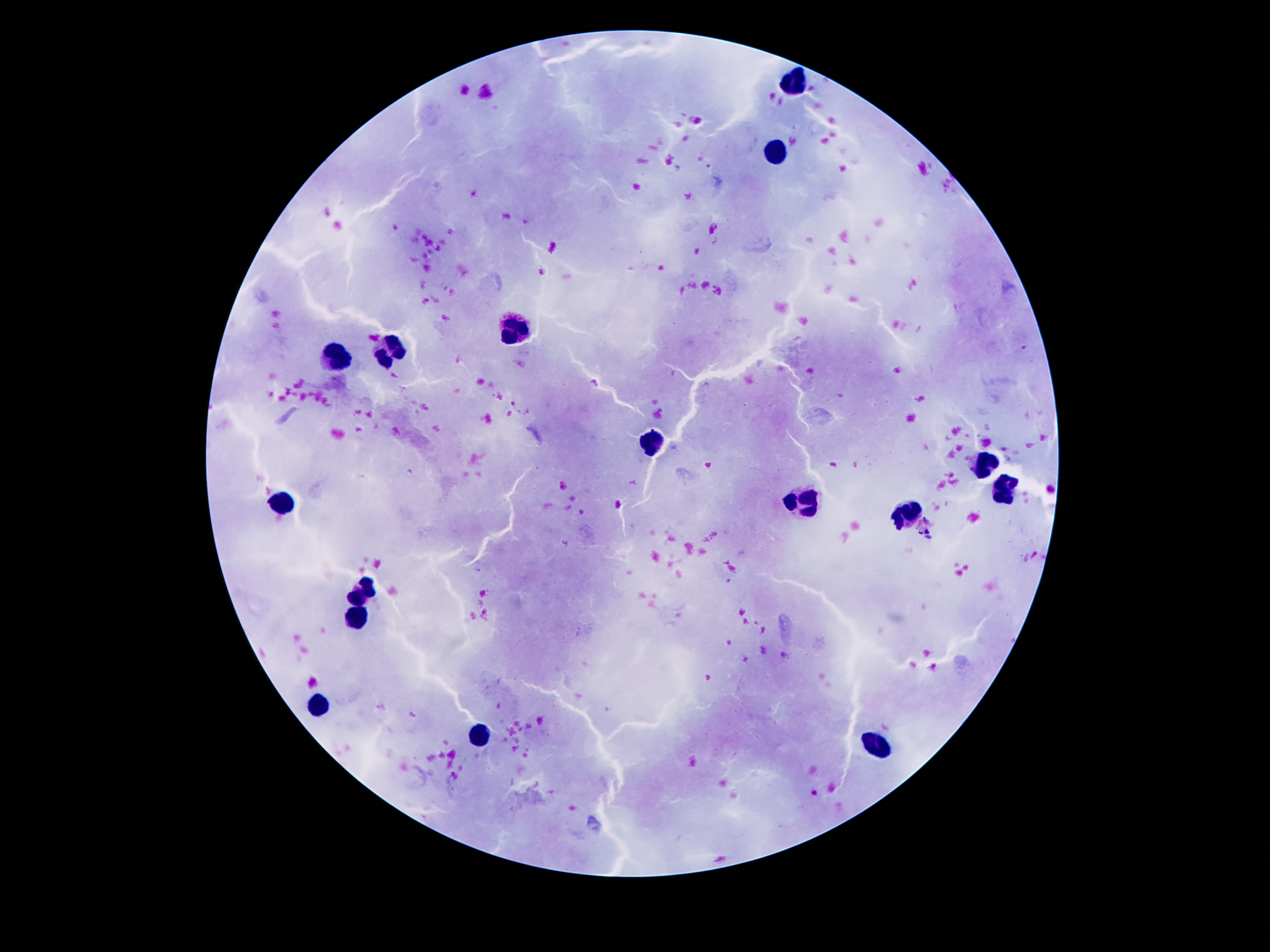

leukocyte locations = approximate centers as {x, y} in pixels: {794, 85}, {773, 152}, {515, 335}, {391, 354}, {336, 362}, {653, 444}, {979, 463}, {1002, 489}, {284, 500}, {805, 501}, {909, 515}, {362, 593}, {358, 621}, {318, 707}, {483, 738}, {874, 746}
stain = Giemsa
image size = 1270×952 pixels
capture = smartphone camera through the microscope eyepiece
preparation = thick peripheral-blood smear
patient malaria status = negative
field of view = one from this slide
magnification = 100x